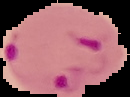

Summary:
  - Image type: cell region segmented out of the field of view; surrounding area masked to black
  - Image size: 130×97 pixels
  - Preparation: thin blood smear
  - Malaria status: parasitized